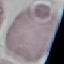

{
  "result": "no malaria parasites seen",
  "image_type": "cell patch, automatically extracted from a larger field of view and resized to 64 × 64 pixels",
  "stain": "Giemsa",
  "capture": "smartphone camera at the microscope eyepiece",
  "preparation": "thin blood smear"
}